Report the malaria status of this cell.
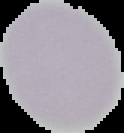

It is uninfected.

image size = 124×133 pixels
image type = cell region segmented out of the field of view; surrounding area masked to black
preparation = thin blood film